State which parasite is depicted.
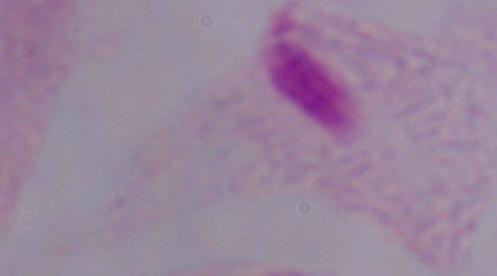
This is a trichomonad.

Photomicrograph. Captured at 1000x magnification.